Name the blood parasite species.
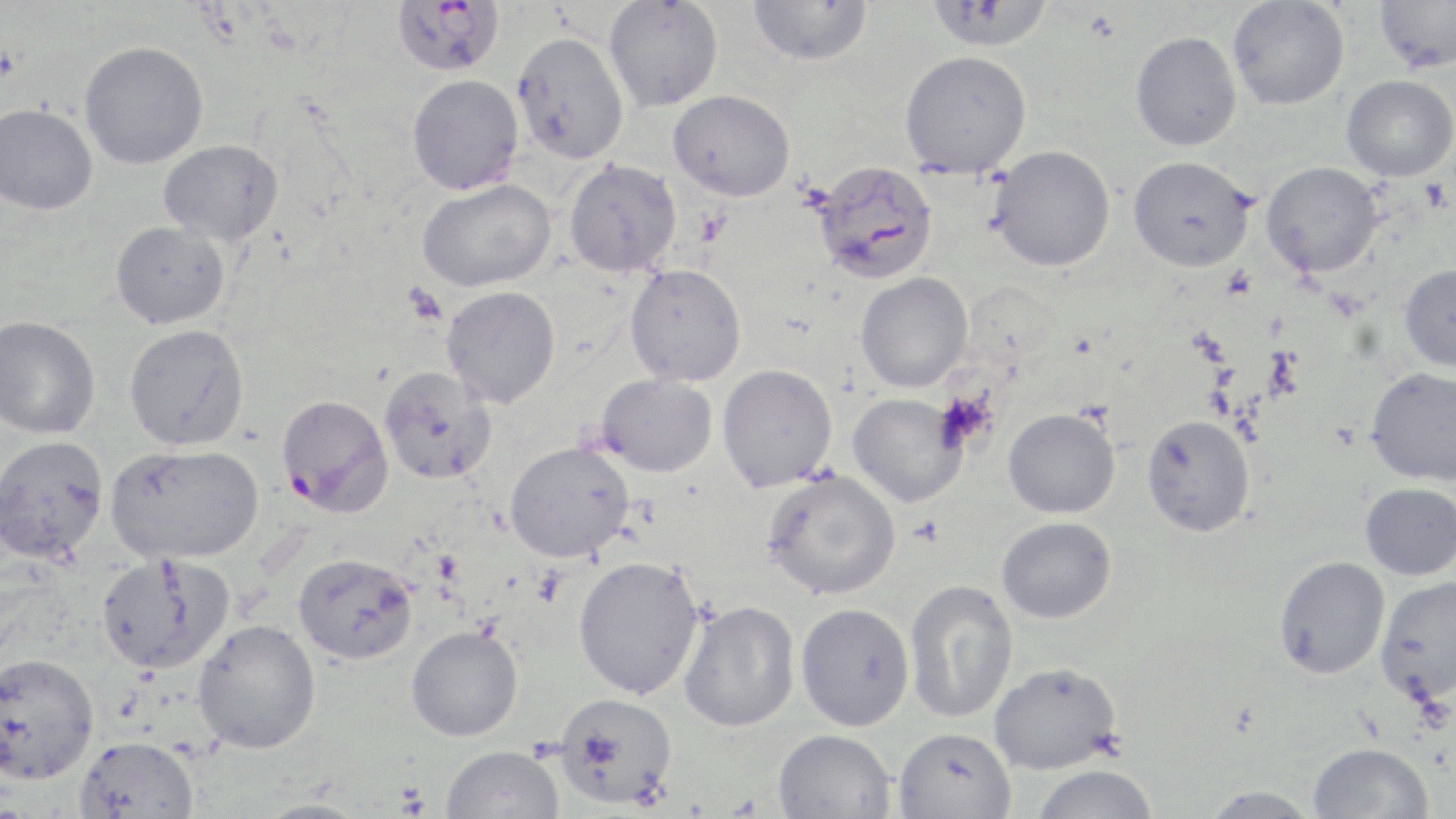

Plasmodium falciparum.

magnification = 1000x
field of view = one of a larger specimen
uninfected red blood cell locations = approximate bounding boxes as named x1/y1/x2/y2 corners in pixels: (x1=604, y1=0, x2=723, y2=112), (x1=748, y1=0, x2=873, y2=66), (x1=926, y1=0, x2=1053, y2=52), (x1=1228, y1=0, x2=1350, y2=110), (x1=1374, y1=0, x2=1456, y2=73), (x1=511, y1=31, x2=629, y2=164), (x1=1130, y1=31, x2=1242, y2=151), (x1=79, y1=40, x2=209, y2=169), (x1=899, y1=50, x2=1032, y2=178), (x1=407, y1=74, x2=524, y2=195), (x1=1342, y1=75, x2=1456, y2=181), (x1=669, y1=89, x2=795, y2=201), (x1=0, y1=103, x2=98, y2=215), (x1=159, y1=139, x2=285, y2=245), (x1=989, y1=144, x2=1116, y2=271), (x1=1128, y1=155, x2=1256, y2=272), (x1=564, y1=158, x2=682, y2=277), (x1=1261, y1=161, x2=1382, y2=276), (x1=417, y1=178, x2=556, y2=292), (x1=111, y1=221, x2=230, y2=328), (x1=624, y1=263, x2=746, y2=387), (x1=1399, y1=265, x2=1456, y2=372), (x1=855, y1=272, x2=973, y2=393), (x1=441, y1=286, x2=561, y2=408), (x1=0, y1=315, x2=100, y2=439), (x1=124, y1=324, x2=249, y2=450), (x1=717, y1=364, x2=837, y2=492), (x1=380, y1=366, x2=498, y2=485), (x1=1366, y1=367, x2=1456, y2=485), (x1=597, y1=373, x2=718, y2=477), (x1=847, y1=393, x2=967, y2=508), (x1=1003, y1=407, x2=1120, y2=518), (x1=1141, y1=414, x2=1255, y2=537), (x1=0, y1=435, x2=109, y2=564), (x1=504, y1=441, x2=634, y2=563), (x1=106, y1=444, x2=263, y2=564), (x1=761, y1=469, x2=901, y2=600), (x1=1360, y1=482, x2=1456, y2=580), (x1=996, y1=516, x2=1116, y2=623), (x1=96, y1=552, x2=233, y2=674), (x1=293, y1=553, x2=418, y2=664), (x1=572, y1=555, x2=705, y2=700), (x1=1274, y1=556, x2=1390, y2=678), (x1=1375, y1=576, x2=1456, y2=703), (x1=904, y1=579, x2=1019, y2=724), (x1=679, y1=599, x2=800, y2=732), (x1=795, y1=602, x2=915, y2=730), (x1=192, y1=619, x2=321, y2=754), (x1=406, y1=624, x2=523, y2=741), (x1=0, y1=651, x2=99, y2=785), (x1=989, y1=661, x2=1122, y2=775), (x1=553, y1=692, x2=678, y2=809), (x1=894, y1=726, x2=1016, y2=818), (x1=773, y1=728, x2=897, y2=819), (x1=75, y1=735, x2=199, y2=819), (x1=1309, y1=742, x2=1433, y2=819), (x1=441, y1=744, x2=565, y2=819), (x1=1029, y1=764, x2=1160, y2=819), (x1=1199, y1=786, x2=1321, y2=818), (x1=254, y1=797, x2=371, y2=818)
image size = 1456×819 pixels
preparation = thin blood film
stain = May-Grünwald-Giemsa
Plasmodium falciparum-infected red blood cell locations = approximate bounding boxes as named x1/y1/x2/y2 corners in pixels: (x1=392, y1=0, x2=505, y2=76), (x1=810, y1=159, x2=939, y2=285), (x1=276, y1=393, x2=393, y2=517)
platelet locations = approximate bounding boxes as named x1/y1/x2/y2 corners in pixels: (x1=0, y1=47, x2=20, y2=81), (x1=908, y1=516, x2=944, y2=546)
modality = optical microscopy